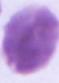
1000x magnification. Micrograph. An erythrocyte is seen.